Identify the blood parasite species.
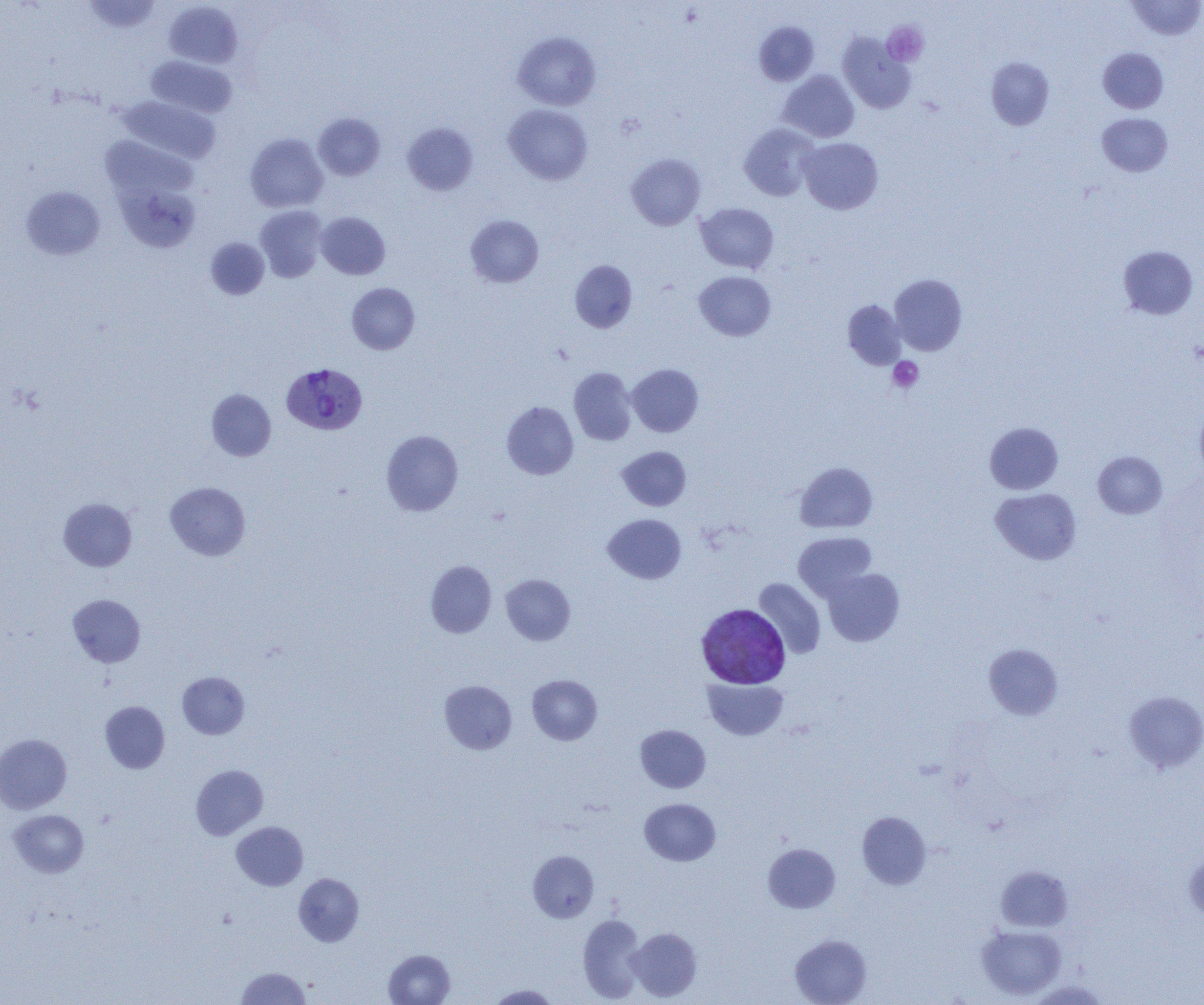

Plasmodium vivax.

uninfected red blood cell locations = approximate bounding boxes as (x1,y1)-(x2,y2) corner pairs in pixels: (82,0)-(163,33), (1127,0)-(1203,41), (163,1)-(243,68), (754,21)-(819,86), (513,32)-(601,110), (838,33)-(916,114), (1098,47)-(1168,113), (146,56)-(238,118), (986,57)-(1054,130), (777,70)-(859,142), (117,96)-(221,164), (503,104)-(593,185), (313,113)-(385,180), (1097,113)-(1172,176), (402,122)-(478,196), (739,123)-(820,201), (245,133)-(328,212), (100,135)-(195,203), (799,137)-(883,214), (626,153)-(705,230), (116,182)-(201,253), (20,186)-(105,260), (696,203)-(778,273), (254,205)-(328,282), (316,212)-(390,279), (466,214)-(544,287), (205,237)-(270,300), (1118,245)-(1199,320), (569,260)-(637,333), (694,271)-(776,341), (890,274)-(967,355), (346,283)-(419,354), (842,300)-(906,369), (627,363)-(703,437), (568,367)-(637,445), (206,389)-(276,461), (501,401)-(578,479), (1195,406)-(1204,482), (984,422)-(1063,494), (381,430)-(463,516), (617,446)-(691,511), (1093,451)-(1167,518), (795,461)-(878,533), (165,482)-(251,560), (990,488)-(1082,565), (58,498)-(137,572), (603,514)-(686,584), (793,531)-(876,600), (425,560)-(496,638), (823,568)-(904,646), (501,574)-(575,645), (753,578)-(826,659), (68,594)-(145,667), (983,643)-(1063,720), (177,671)-(249,739), (527,674)-(602,745), (702,678)-(789,740), (439,680)-(517,754), (1125,690)-(1204,772), (100,701)-(169,773), (635,725)-(710,792), (0,734)-(72,814), (191,764)-(268,840), (640,798)-(720,866), (8,810)-(88,877), (857,811)-(931,889), (231,821)-(308,890), (763,843)-(840,913), (528,850)-(599,922), (1184,853)-(1204,920), (996,865)-(1073,932), (294,873)-(364,946), (578,914)-(646,1002), (977,925)-(1066,999), (628,927)-(702,1001), (790,934)-(872,1005), (383,949)-(455,1005), (236,966)-(311,1005), (1026,980)-(1110,1004), (487,984)-(560,1004)
platelet locations = approximate bounding boxes as (x1,y1)-(x2,y2) corner pairs in pixels: (882,22)-(928,66), (888,356)-(924,393)
field of view = one of a larger specimen
image size = 1204×1005 pixels
magnification = 1000x
Plasmodium vivax-infected red blood cell locations = approximate bounding boxes as (x1,y1)-(x2,y2) corner pairs in pixels: (281,362)-(368,436), (696,604)-(791,688)
modality = optical microscopy
preparation = thin blood smear